Outline every leukocyte.
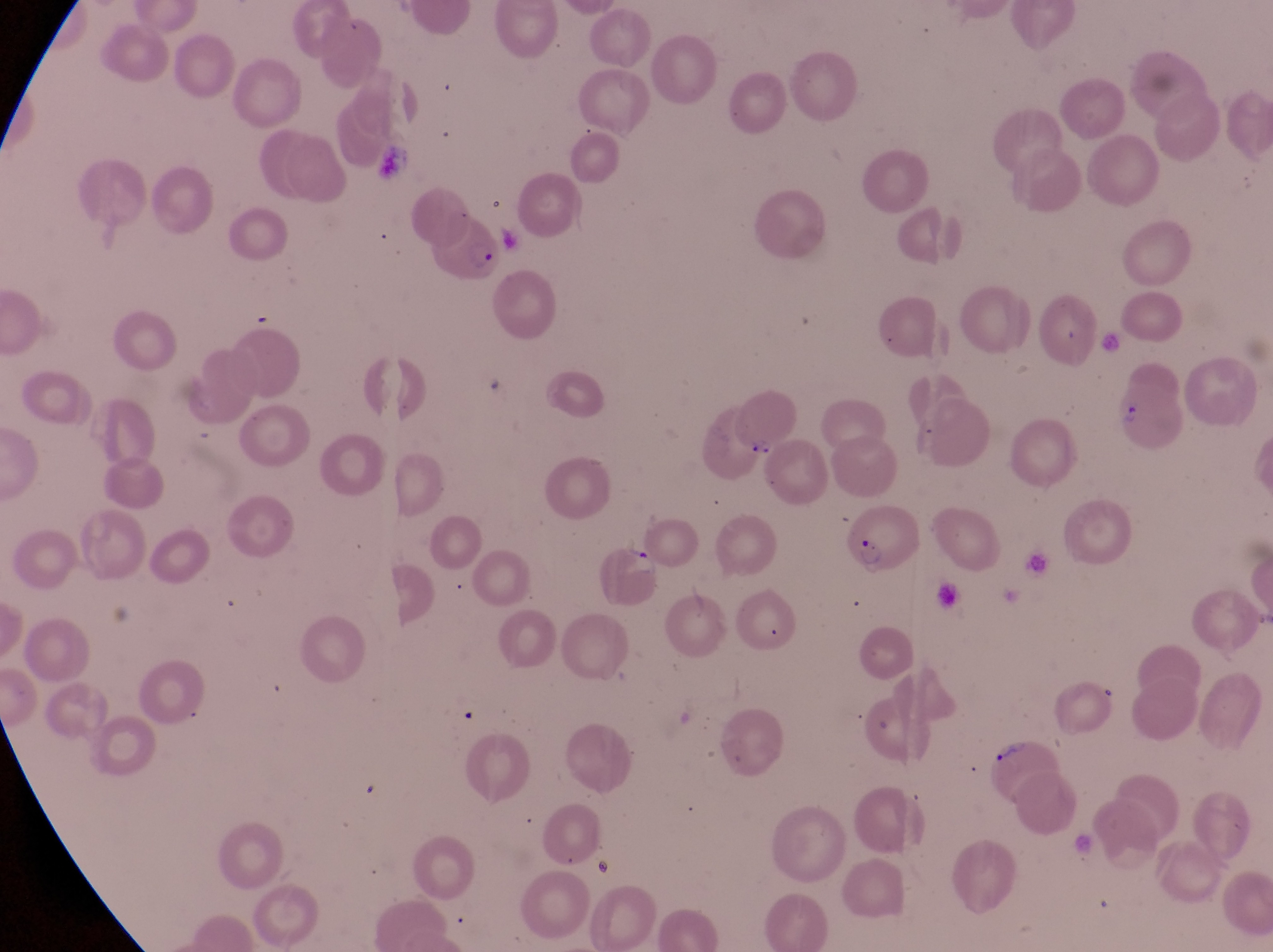

No leukocytes observed.

capture = smartphone photograph through the eyepiece of an Olympus CX-23 microscope
preparation = thin blood film
artifact (platelet-like body, stain precipitate, or debris) locations = approximate bounding boxes as (left, top, right, bottom) in pixels: (369, 148, 421, 193), (993, 741, 1025, 763)
field of view = single
image size = 1273×952 pixels
parasitised red blood cell locations = approximate bounding boxes as (left, top, right, bottom) in pixels: (426, 218, 504, 283), (1113, 385, 1198, 462), (839, 509, 917, 576), (599, 543, 666, 609)
magnification = 1000x
country = Uganda